Classify this cell by malaria status.
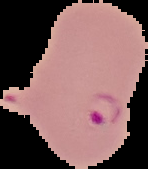

It is parasitized.

Cell region segmented out of the field of view; the surrounding area is masked to black. Image is 148×169 pixels. From a thin blood film.